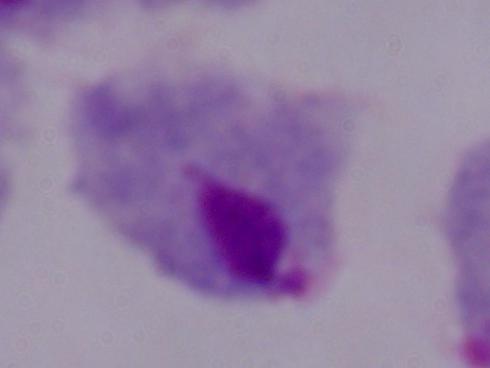

Summary:
  - Modality: micrograph
  - Identification: trichomonad
  - Magnification: 1000x